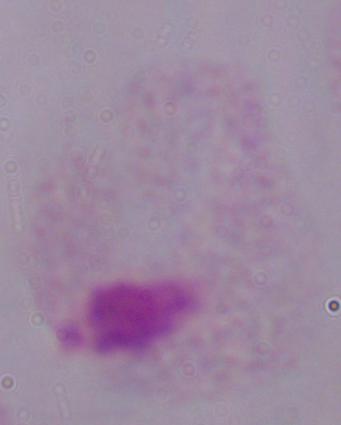 Captured at 1000x magnification. Photomicrograph. A trichomonad is shown.